Comment on the morphology of the red blood cells.
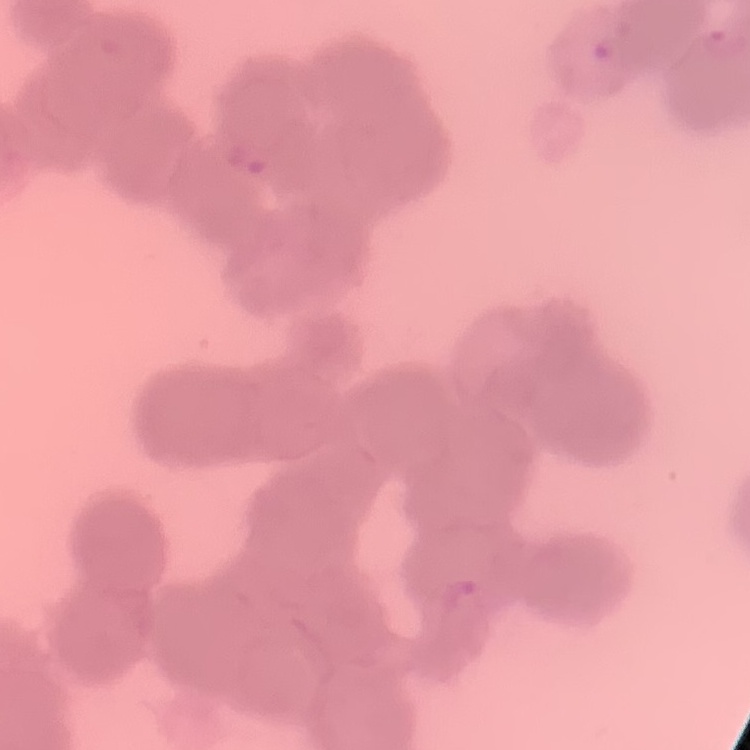

They show rouleaux formation.

Field's or Giemsa stain. Square crop of a larger photomicrograph. Thin blood smear.